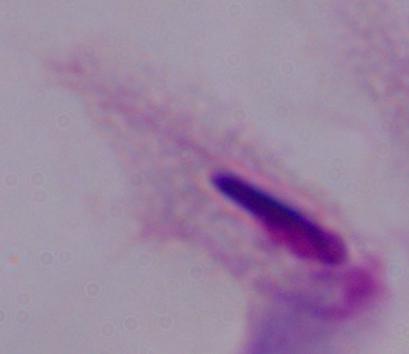 1000x magnification. Micrograph. A trichomonad is seen.